Point out each Plasmodium parasite.
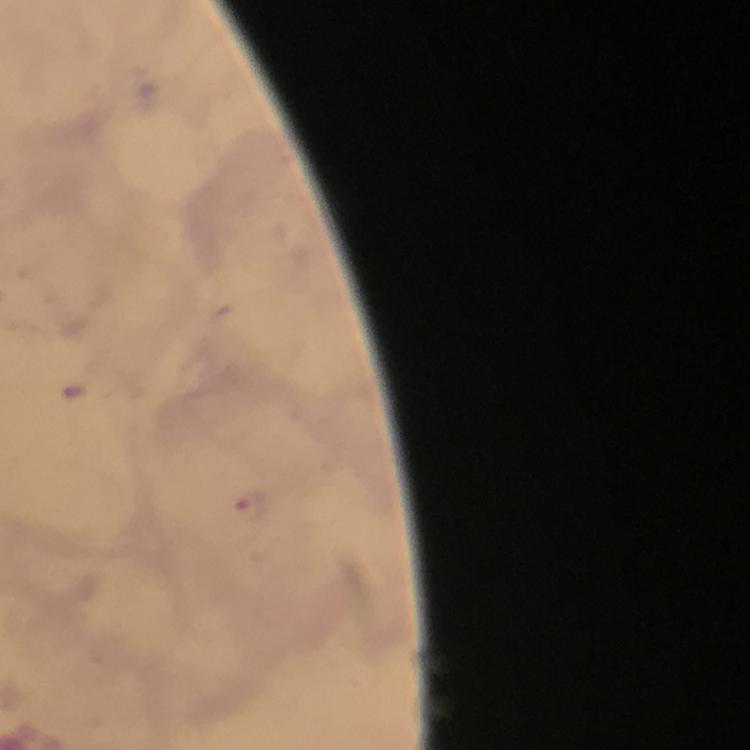
Approximate centers as (x, y) in pixels.
Plasmodium parasites: (251, 503).

Photographed through the microscope with a smartphone camera. Immersion oil applied. A crop from one field of view. Thick smear. From a diagnostic examination for malaria. Image is 750×750 pixels. Giemsa-stained preparation. 100x magnification.